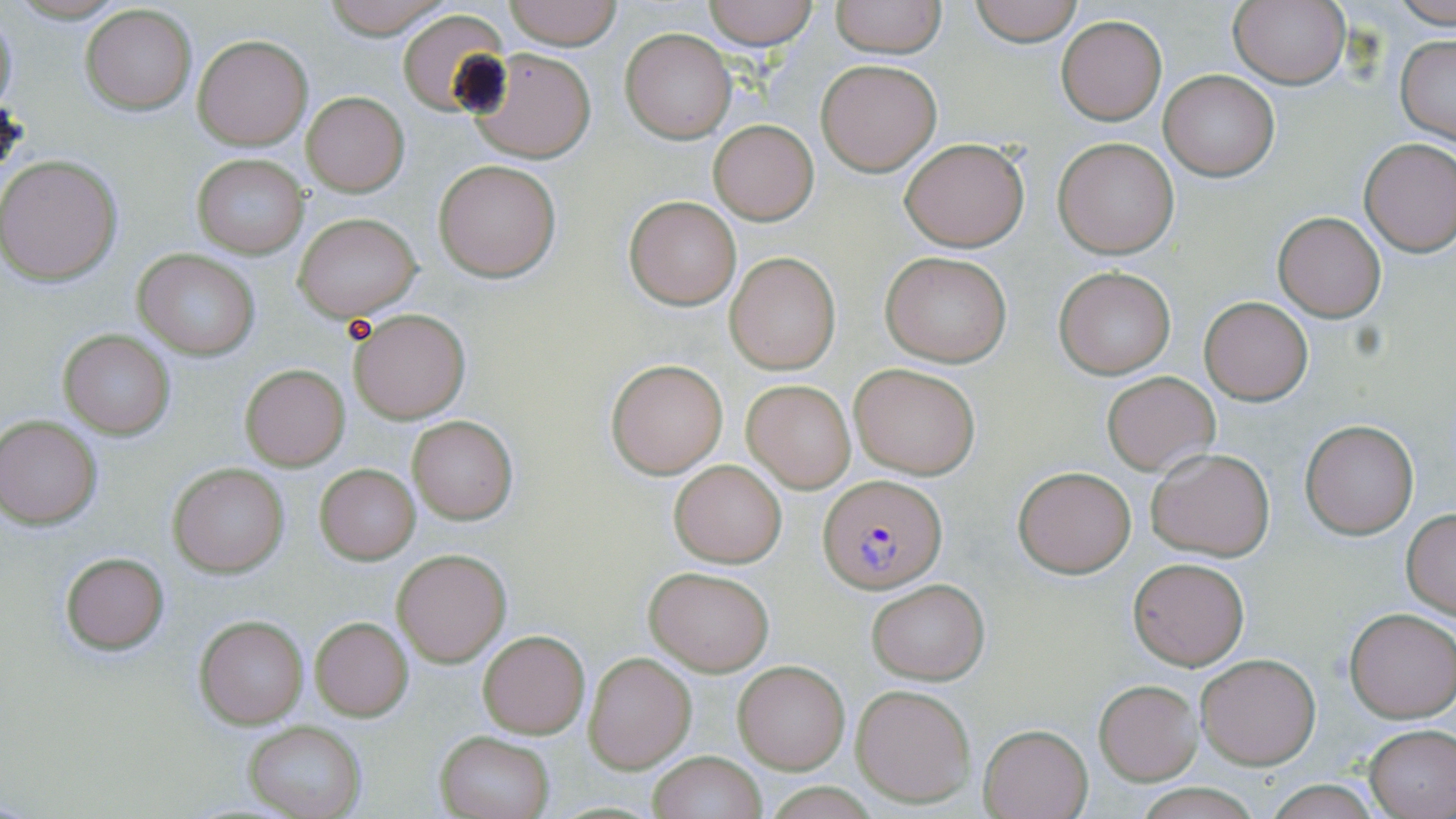 Approximate bounding boxes as (x1,y1)-(x2,y2) corner pairs in pixels. Plasmodium falciparum-infected red blood cell locations: (821,474)-(947,593). Uninfected red blood cell locations: (318,0)-(455,39), (501,0)-(623,49), (702,0)-(819,49), (830,0)-(947,57), (966,0)-(1086,45), (1389,0)-(1456,26), (1228,1)-(1350,89), (81,5)-(197,114), (398,10)-(509,115), (0,11)-(20,116), (1057,15)-(1166,124), (621,28)-(735,143), (192,34)-(313,150), (1394,34)-(1456,143), (466,47)-(598,163), (816,59)-(941,176), (1159,69)-(1279,181), (302,92)-(409,196), (709,120)-(818,225), (1053,136)-(1181,258), (900,137)-(1029,251), (1359,137)-(1456,256), (192,154)-(309,258), (0,155)-(123,286), (435,160)-(561,281), (623,194)-(743,309), (1274,211)-(1386,321), (292,212)-(423,320), (133,249)-(260,359), (881,251)-(1013,367), (725,253)-(840,373), (1053,266)-(1177,379), (1199,296)-(1314,404), (346,307)-(470,423), (57,327)-(177,441), (606,360)-(727,476), (849,361)-(982,479), (239,363)-(351,472), (1100,370)-(1219,475), (741,379)-(857,493), (408,415)-(518,525), (1,416)-(103,527), (1300,421)-(1418,538), (1146,447)-(1276,561), (668,458)-(787,568), (169,463)-(289,578), (316,464)-(419,563), (1013,465)-(1136,577), (1401,510)-(1456,618), (393,549)-(511,667), (58,550)-(171,655), (1129,556)-(1249,669), (645,567)-(774,675), (867,579)-(989,684), (1344,608)-(1456,721), (194,613)-(310,729), (309,618)-(414,720), (478,629)-(589,739), (584,652)-(696,773), (1196,653)-(1321,769), (734,660)-(850,773), (1094,679)-(1202,785), (851,683)-(976,806), (241,720)-(366,819), (978,724)-(1093,819), (1364,724)-(1456,819), (435,731)-(554,818), (647,751)-(765,819), (1259,781)-(1385,816). Slide-level diagnosis: Plasmodium falciparum. Optical microscopy. Single field of view. Image is 1456×819 pixels. Captured at 1000x magnification. Thin blood film. May-Grünwald-Giemsa-stained preparation.